Identify the parasite.
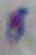
Toxoplasma gondii.

magnification = 1000x
modality = micrograph